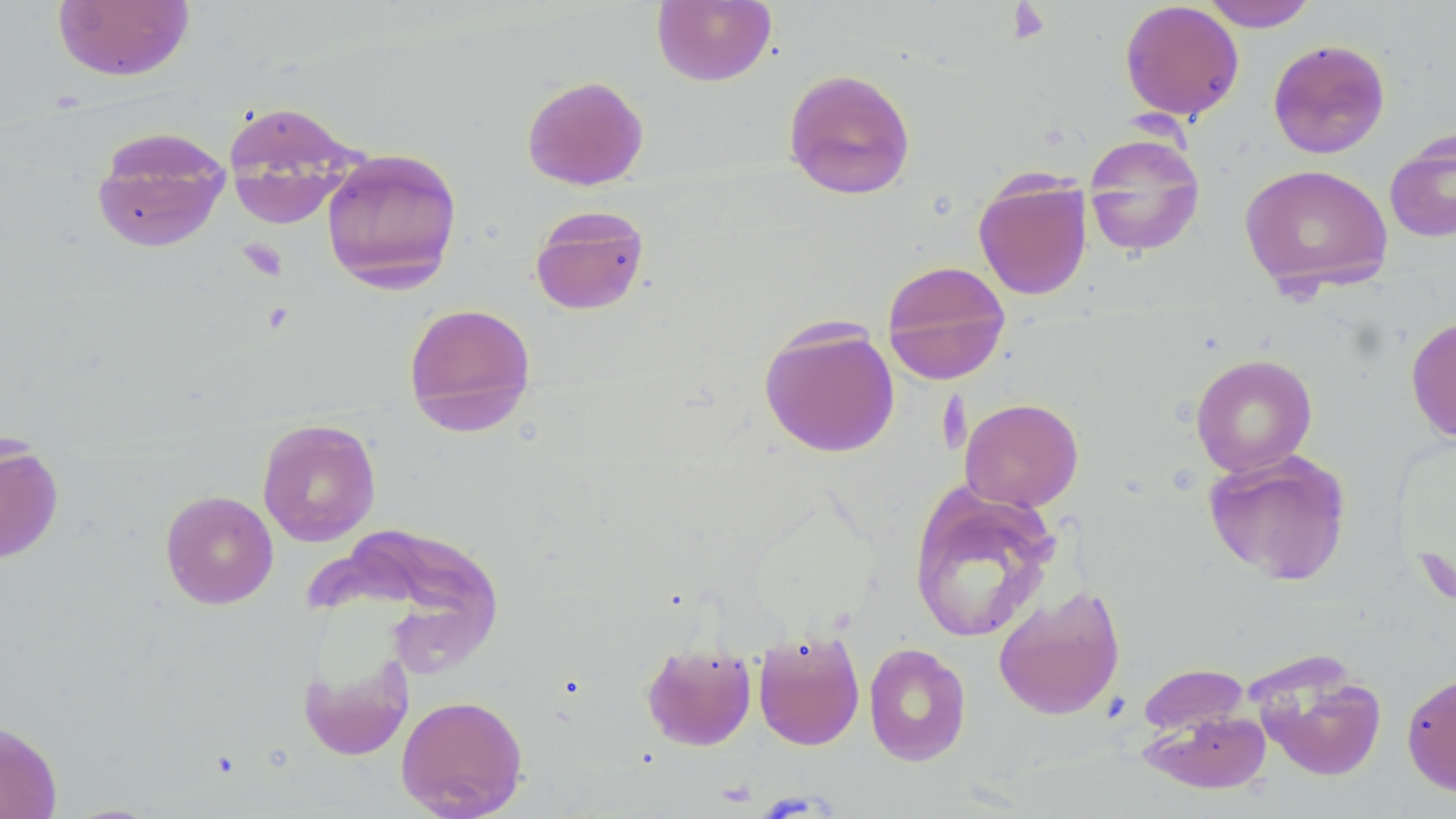

Approximate bounding boxes as named x1/y1/x2/y2 corners in pixels. Uninfected red blood cell locations: (x1=651, y1=0, x2=777, y2=87), (x1=1199, y1=0, x2=1319, y2=31), (x1=51, y1=1, x2=195, y2=82), (x1=1119, y1=1, x2=1244, y2=121), (x1=1267, y1=39, x2=1391, y2=159), (x1=782, y1=67, x2=916, y2=200), (x1=522, y1=75, x2=649, y2=191), (x1=222, y1=101, x2=363, y2=229), (x1=91, y1=127, x2=231, y2=254), (x1=1384, y1=128, x2=1456, y2=243), (x1=1082, y1=132, x2=1206, y2=258), (x1=320, y1=147, x2=463, y2=293), (x1=1239, y1=164, x2=1394, y2=296), (x1=973, y1=173, x2=1093, y2=300), (x1=530, y1=205, x2=650, y2=316), (x1=881, y1=259, x2=1011, y2=384), (x1=403, y1=302, x2=536, y2=435), (x1=1405, y1=314, x2=1456, y2=444), (x1=758, y1=320, x2=900, y2=458), (x1=1190, y1=353, x2=1318, y2=477), (x1=959, y1=397, x2=1084, y2=512), (x1=257, y1=418, x2=381, y2=547), (x1=0, y1=438, x2=64, y2=564), (x1=1203, y1=449, x2=1353, y2=587), (x1=908, y1=483, x2=1061, y2=643), (x1=160, y1=489, x2=279, y2=609), (x1=993, y1=584, x2=1126, y2=721), (x1=753, y1=628, x2=865, y2=751), (x1=641, y1=642, x2=757, y2=751), (x1=863, y1=642, x2=972, y2=766), (x1=298, y1=648, x2=415, y2=763), (x1=1137, y1=663, x2=1250, y2=735), (x1=1256, y1=664, x2=1387, y2=781), (x1=1402, y1=670, x2=1456, y2=796), (x1=396, y1=693, x2=528, y2=818), (x1=1141, y1=710, x2=1272, y2=794), (x1=0, y1=719, x2=62, y2=819). Platelet locations: (x1=1006, y1=3, x2=1053, y2=44), (x1=238, y1=238, x2=288, y2=282). Slide-level diagnosis: negative for blood parasites. Optical microscopy. May-Grünwald-Giemsa-stained preparation. Single field of view. Image is 1456×819 pixels. Thin blood smear. 1000x magnification.